Assess this cell for malaria.
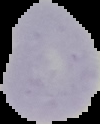
It is uninfected.

From a thin blood film. The area outside the segmented cell region is set to black. Image is 100×124 pixels.